Comment on the morphology of the red blood cells.
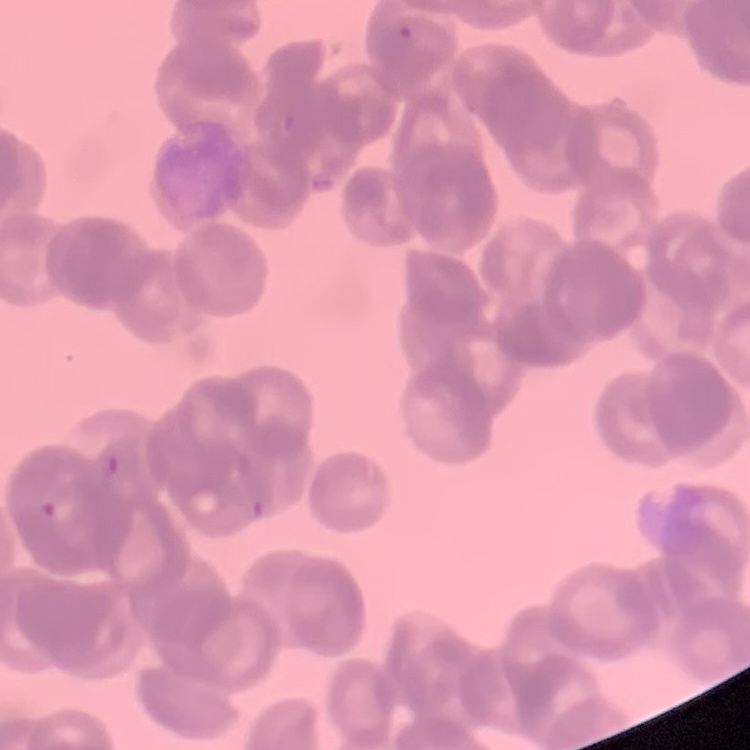
They show rouleaux formation.

Summary:
  - Stain: Field's or Giemsa
  - Preparation: thin blood film
  - Image type: square crop of a larger photomicrograph